Identify the cell.
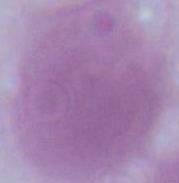
This is an erythrocyte.

Summary:
  - Magnification: 1000x
  - Modality: micrograph